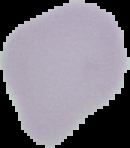
From a thin blood smear. Image is 130×148 pixels. Segmented cell region on a black background. Result: no Plasmodium parasites seen.